Assess this cell for malaria.
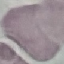
It is uninfected.

capture = smartphone through the microscope eyepiece
stain = Giemsa
image type = automatically extracted cell patch, resized to 64 × 64 pixels
preparation = thin blood smear